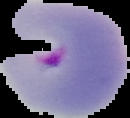
Summary:
  - Result: malaria parasites identified
  - Image size: 130×118 pixels
  - Preparation: thin blood film
  - Image type: cell region segmented out of the field of view; surrounding area masked to black